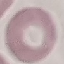
Summary:
  - Malaria status: uninfected
  - Image type: automatically extracted cell patch, resized to 64 × 64 pixels
  - Capture: smartphone through the microscope eyepiece
  - Stain: Giemsa
  - Preparation: thin blood smear